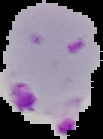 From a thin blood smear. Cell region segmented out of the field of view; the surrounding area is masked to black. Image is 103×139 pixels. Malaria status: parasitized.